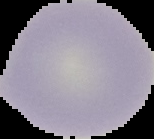

Result: negative for Plasmodium parasites. Image is 154×139 pixels. From a thin blood film. The area outside the segmented cell region is set to black.